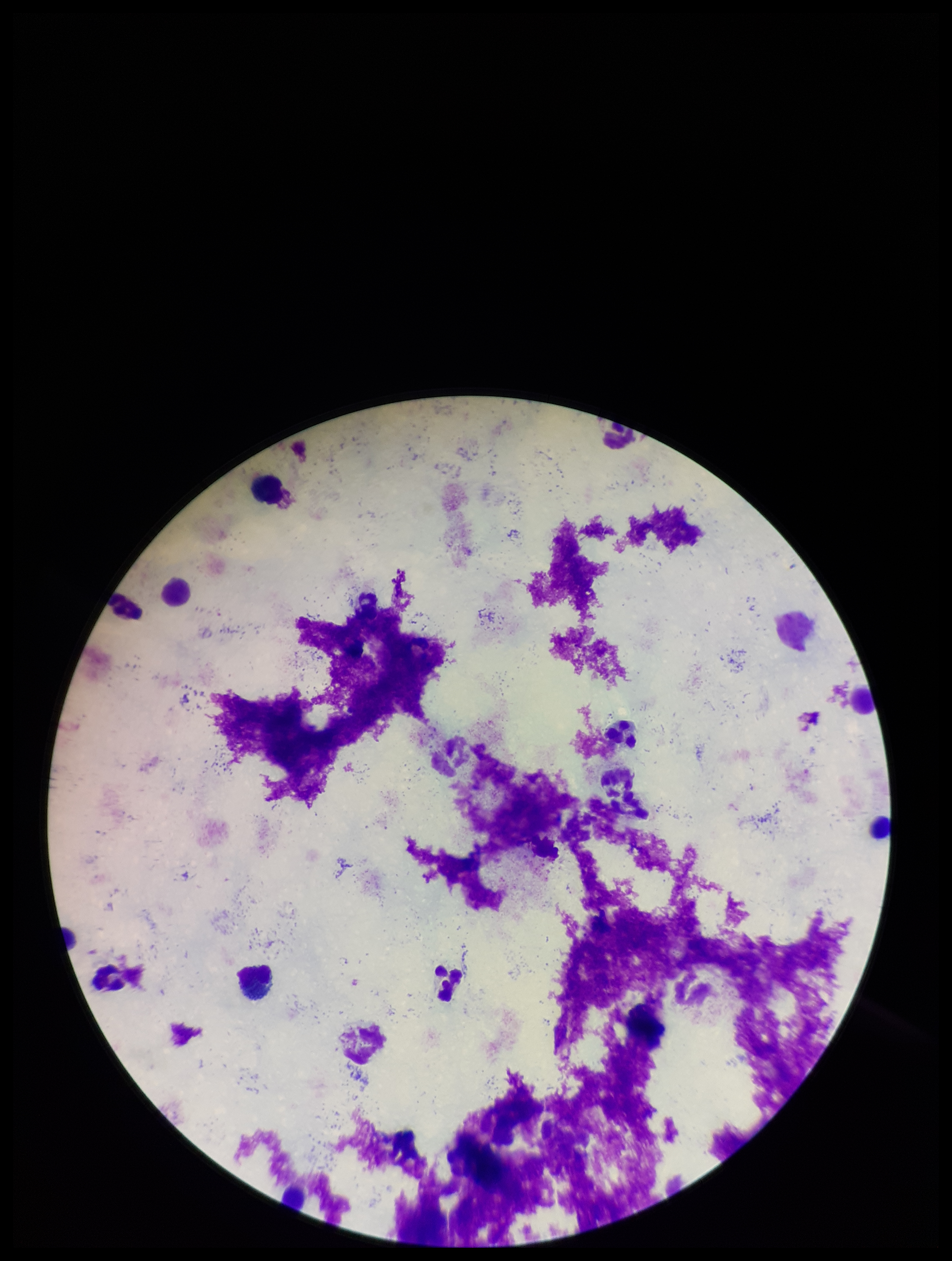

Summary:
  - Image size: 952×1261 pixels
  - Plasmodium parasites: none identified
  - Leukocyte count: 7
  - Capture: smartphone photograph through the microscope eyepiece
  - Stain: Giemsa
  - Parasite count: 0
  - Preparation: thick smear
  - Patient malaria status: negative
  - Field of view: single